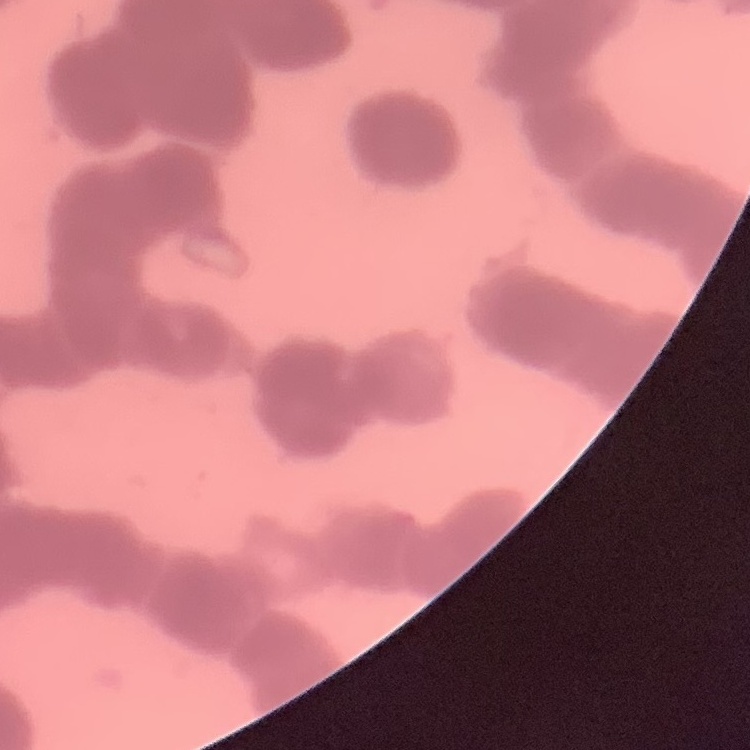
Summary:
  - Red blood cell morphology: rouleaux formation
  - Image type: one tile cut from a larger photomicrograph
  - Stain: Field's or Giemsa
  - Preparation: thin blood film